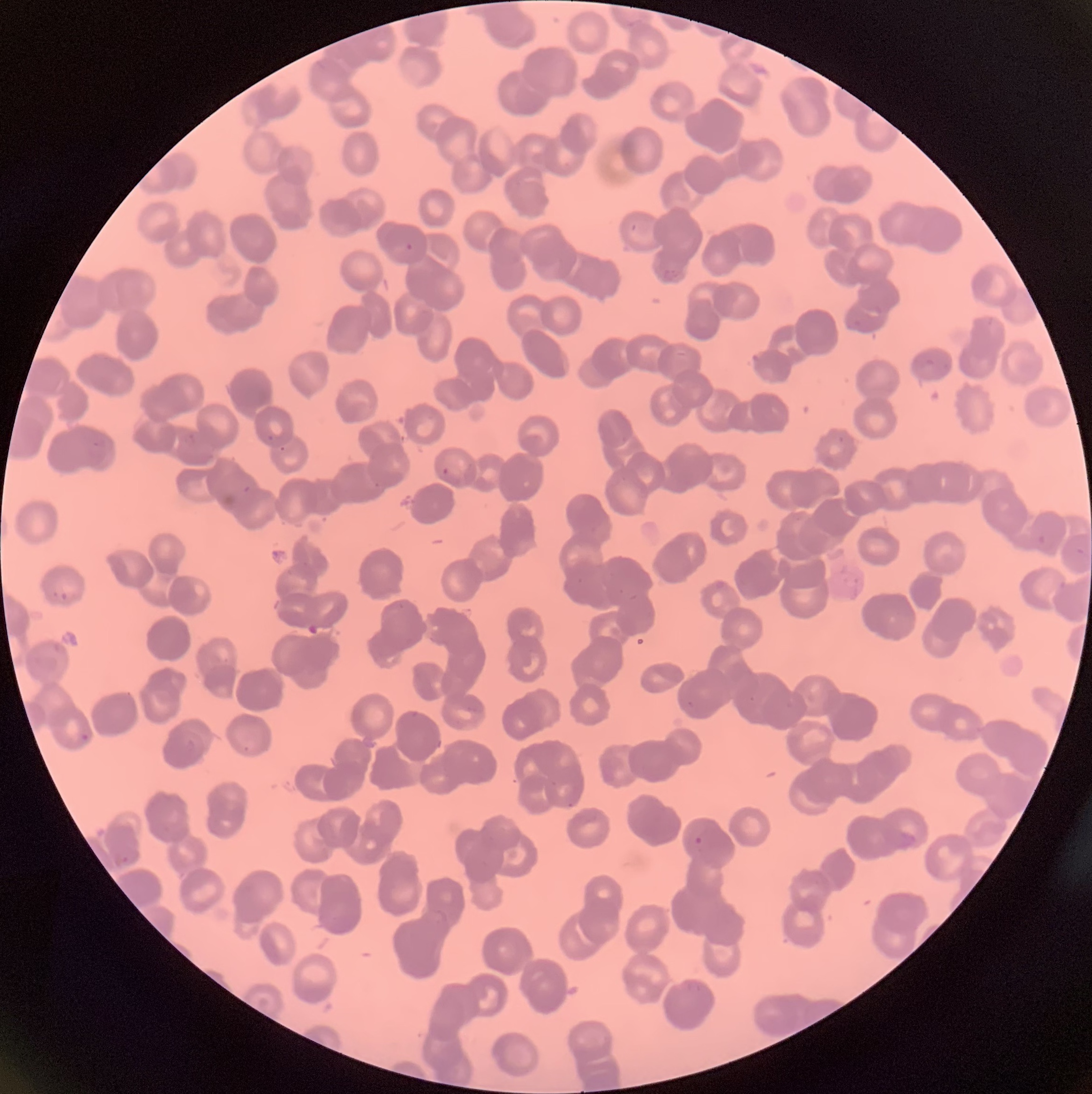

coordinate format = approximate bounding boxes as (x1, y1, x2, y2) in pixels
Plasmodium parasite locations = (405, 242, 414, 252), (660, 269, 680, 284), (183, 432, 196, 446), (92, 441, 100, 448), (278, 445, 287, 453), (441, 466, 451, 476), (373, 482, 382, 490), (242, 485, 252, 495), (1036, 534, 1047, 546), (1074, 546, 1087, 558), (713, 578, 730, 593), (1057, 579, 1069, 590), (52, 590, 70, 602), (52, 640, 64, 655), (747, 694, 756, 703), (686, 699, 696, 709), (785, 700, 797, 712), (80, 732, 90, 742), (186, 737, 196, 751), (243, 745, 251, 753), (549, 780, 559, 788), (565, 801, 576, 809), (897, 830, 919, 850), (693, 835, 704, 846), (113, 853, 129, 868), (683, 979, 703, 993)
Plasmodium parasites too small for a box (approximate centers as (x, y) in pixels) = (270, 438), (841, 439)
preparation = thin blood smear
modality = light microscopy
image size = 1092×1094 pixels
red blood cell morphology = rouleaux formation